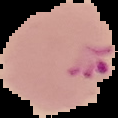 From a thin blood smear. Segmented cell region on a black background. Image is 118×118 pixels. Result: Plasmodium parasites detected.